State the blood parasite species.
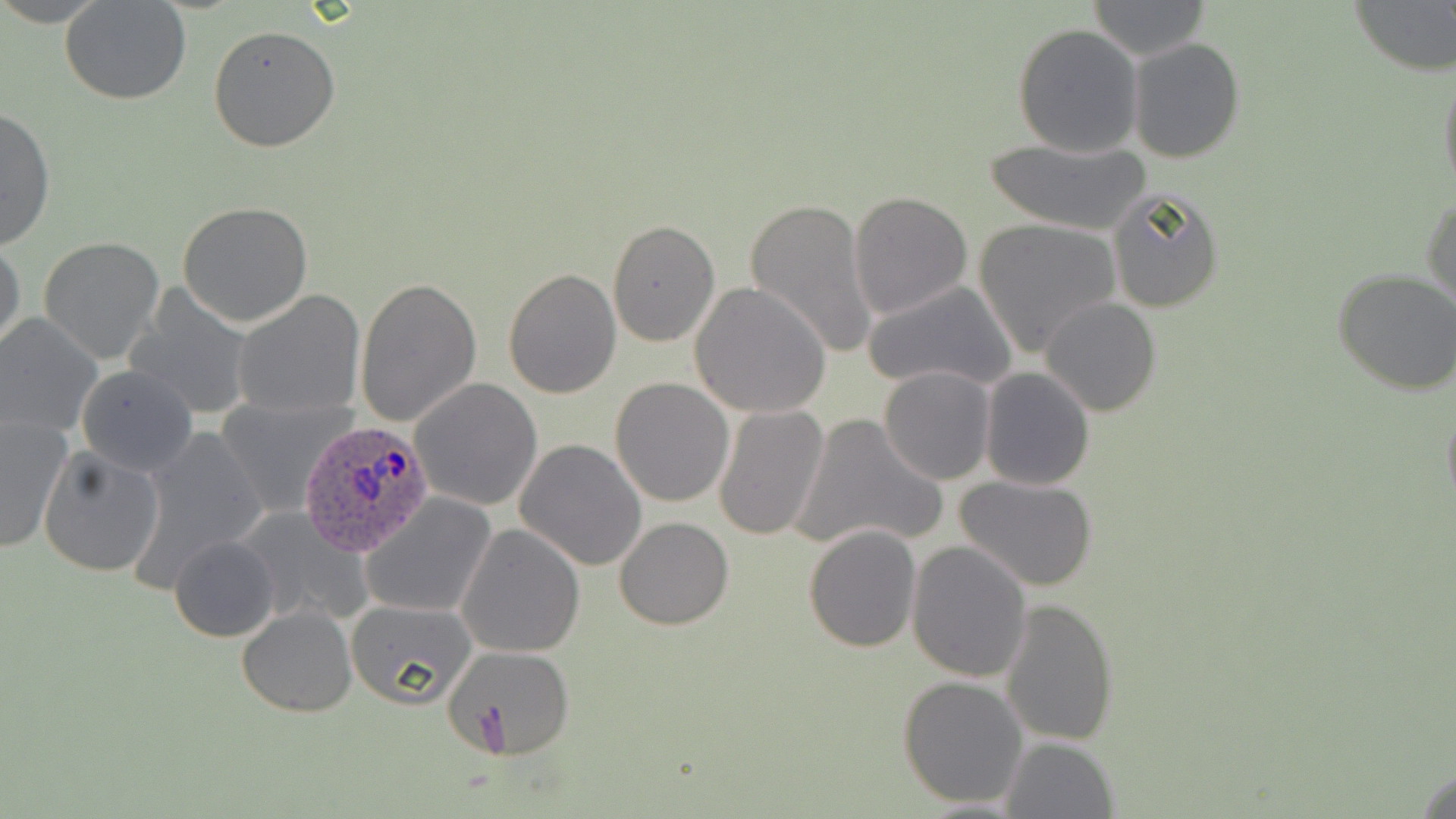

Plasmodium ovale.

Summary:
  - Coordinate format: approximate bounding boxes as (x1,y1)-(x2,y2) corner pairs in pixels
  - Uninfected red blood cell locations: (1349,0)-(1456,74), (61,1)-(192,105), (1084,1)-(1209,59), (1013,23)-(1143,157), (209,24)-(341,153), (1129,37)-(1247,163), (1439,64)-(1456,201), (0,105)-(55,251), (980,135)-(1154,236), (1107,187)-(1224,314), (848,190)-(974,322), (1423,194)-(1455,314), (744,196)-(878,360), (177,201)-(313,326), (607,218)-(720,349), (972,218)-(1120,356), (38,235)-(166,365), (0,238)-(25,358), (1333,268)-(1456,395), (503,269)-(621,399), (355,277)-(481,428), (861,278)-(1018,396), (689,282)-(832,418), (124,287)-(260,421), (232,289)-(365,416), (1040,297)-(1162,418), (0,313)-(101,440), (76,364)-(196,476), (879,366)-(996,483), (979,367)-(1096,491), (610,377)-(735,507), (411,378)-(542,511), (1441,396)-(1456,518), (213,397)-(355,518), (713,404)-(830,542), (790,413)-(948,554), (0,419)-(71,549), (126,425)-(269,587), (515,438)-(647,572), (37,447)-(166,577), (956,473)-(1100,591), (359,493)-(498,620), (235,505)-(372,629), (614,516)-(734,632), (456,523)-(586,658), (804,524)-(923,652), (168,535)-(280,642), (906,541)-(1034,683), (1001,597)-(1119,746), (346,598)-(478,708), (238,605)-(358,716), (439,645)-(574,759), (896,675)-(1028,809), (998,735)-(1120,818), (1411,763)-(1456,819)
  - Plasmodium ovale-infected red blood cell locations: (299,418)-(434,557)
  - Stain: May-Grünwald-Giemsa
  - Image size: 1456×819 pixels
  - Field of view: single
  - Magnification: 1000x
  - Modality: light microscopy
  - Preparation: thin blood film